Give the extent of all Plasmodium falciparum-infected red blood cells.
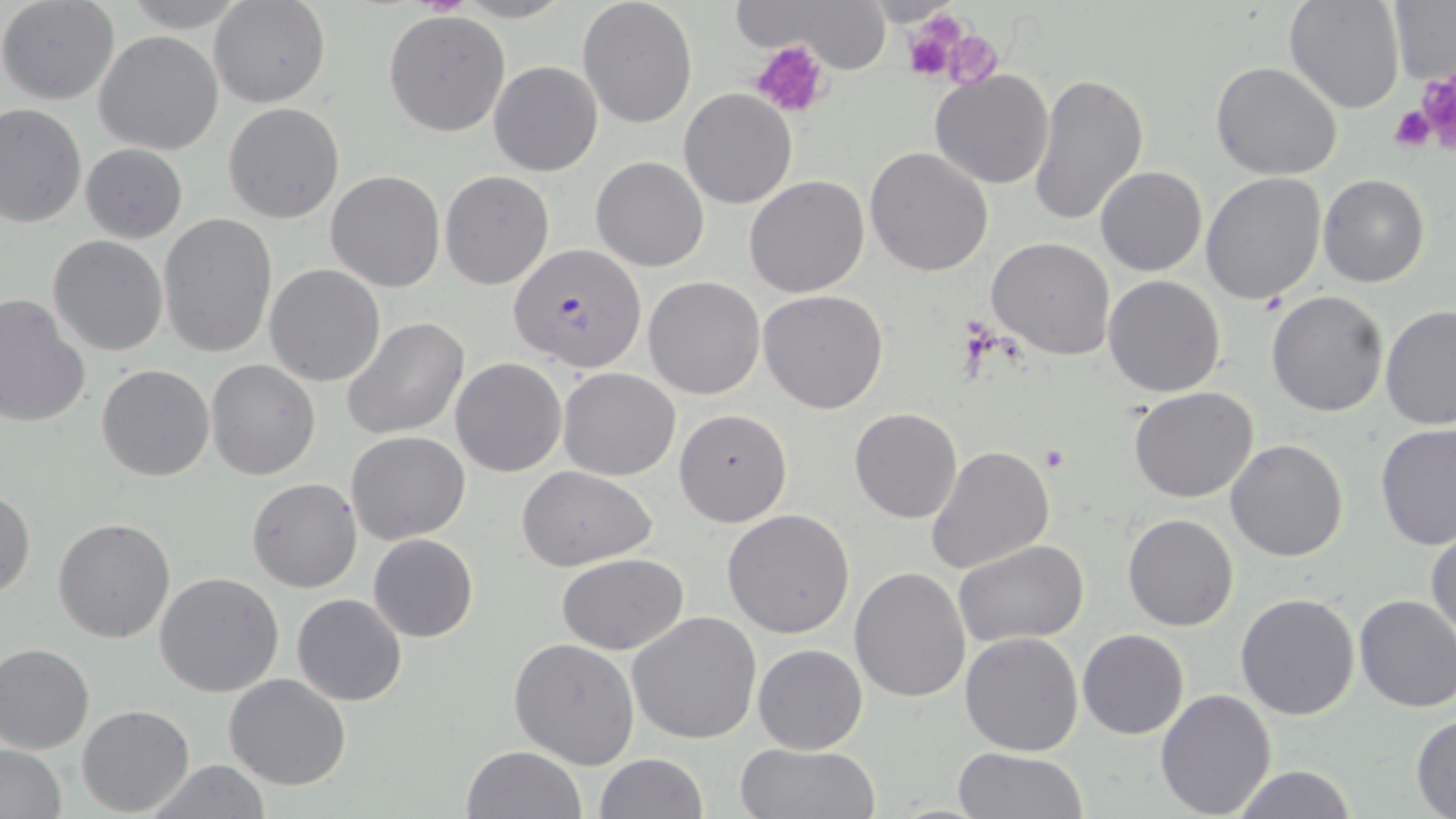

Approximate bounding boxes as (x1, y1, x2, y2) in pixels.
Plasmodium falciparum-infected red blood cells: (507, 243, 648, 374).

Uninfected red blood cell locations: (0, 0, 120, 105), (119, 0, 250, 32), (210, 0, 329, 107), (577, 0, 698, 129), (738, 0, 900, 71), (1284, 0, 1404, 114), (1387, 3, 1455, 87), (383, 10, 511, 135), (93, 31, 223, 155), (489, 61, 602, 176), (1210, 61, 1343, 181), (929, 70, 1055, 189), (1026, 71, 1147, 226), (678, 88, 796, 209), (223, 103, 344, 223), (0, 104, 86, 227), (80, 143, 187, 243), (865, 147, 994, 278), (591, 155, 709, 271), (1096, 166, 1207, 277), (326, 170, 445, 291), (440, 170, 553, 290), (1200, 172, 1325, 303), (744, 175, 871, 298), (1320, 175, 1431, 289), (157, 212, 279, 359), (47, 235, 169, 357), (986, 237, 1115, 359), (264, 263, 386, 386), (1103, 274, 1227, 397), (643, 276, 764, 399), (759, 289, 889, 413), (1266, 291, 1389, 417), (0, 293, 92, 430), (1380, 304, 1455, 430), (341, 317, 471, 441), (450, 358, 566, 477), (205, 359, 321, 479), (96, 364, 215, 481), (557, 367, 681, 480), (1128, 386, 1259, 503), (673, 408, 793, 527), (849, 408, 962, 524), (1374, 422, 1456, 551), (346, 431, 470, 545), (1225, 439, 1348, 561), (926, 445, 1056, 576), (518, 467, 659, 570), (247, 477, 362, 592), (0, 487, 36, 600), (722, 509, 855, 640), (1123, 512, 1239, 632), (52, 517, 177, 644), (1427, 528, 1456, 647), (368, 533, 478, 642), (954, 538, 1088, 647), (556, 552, 689, 656), (849, 565, 971, 703), (153, 571, 285, 698), (1235, 592, 1362, 721), (291, 593, 407, 707), (1353, 594, 1456, 714), (628, 611, 762, 744), (1078, 629, 1188, 740), (959, 631, 1086, 756), (508, 637, 641, 770), (0, 642, 94, 754), (752, 642, 869, 754), (223, 674, 351, 791), (1155, 687, 1278, 817), (79, 705, 195, 815), (1410, 715, 1455, 817), (734, 742, 881, 819), (0, 744, 68, 819), (462, 745, 585, 819), (953, 747, 1087, 819), (594, 752, 707, 819), (144, 760, 273, 818), (1226, 765, 1358, 819). Platelet locations: (901, 13, 966, 83), (941, 30, 1003, 90), (752, 39, 832, 118), (1415, 71, 1456, 153), (1390, 104, 1440, 152), (1038, 446, 1068, 473). Slide-level diagnosis: Plasmodium falciparum. Thin blood smear. Image is 1456×819 pixels. May-Grünwald-Giemsa-stained preparation. Captured at 1000x magnification. Optical microscopy. One field of a larger specimen.